Report the malaria status of this cell.
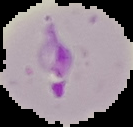

Parasitized.

preparation: thin blood film
image_size: 133×127 pixels
image_type: segmented cell region with the area outside set to black